Locate every Plasmodium parasite.
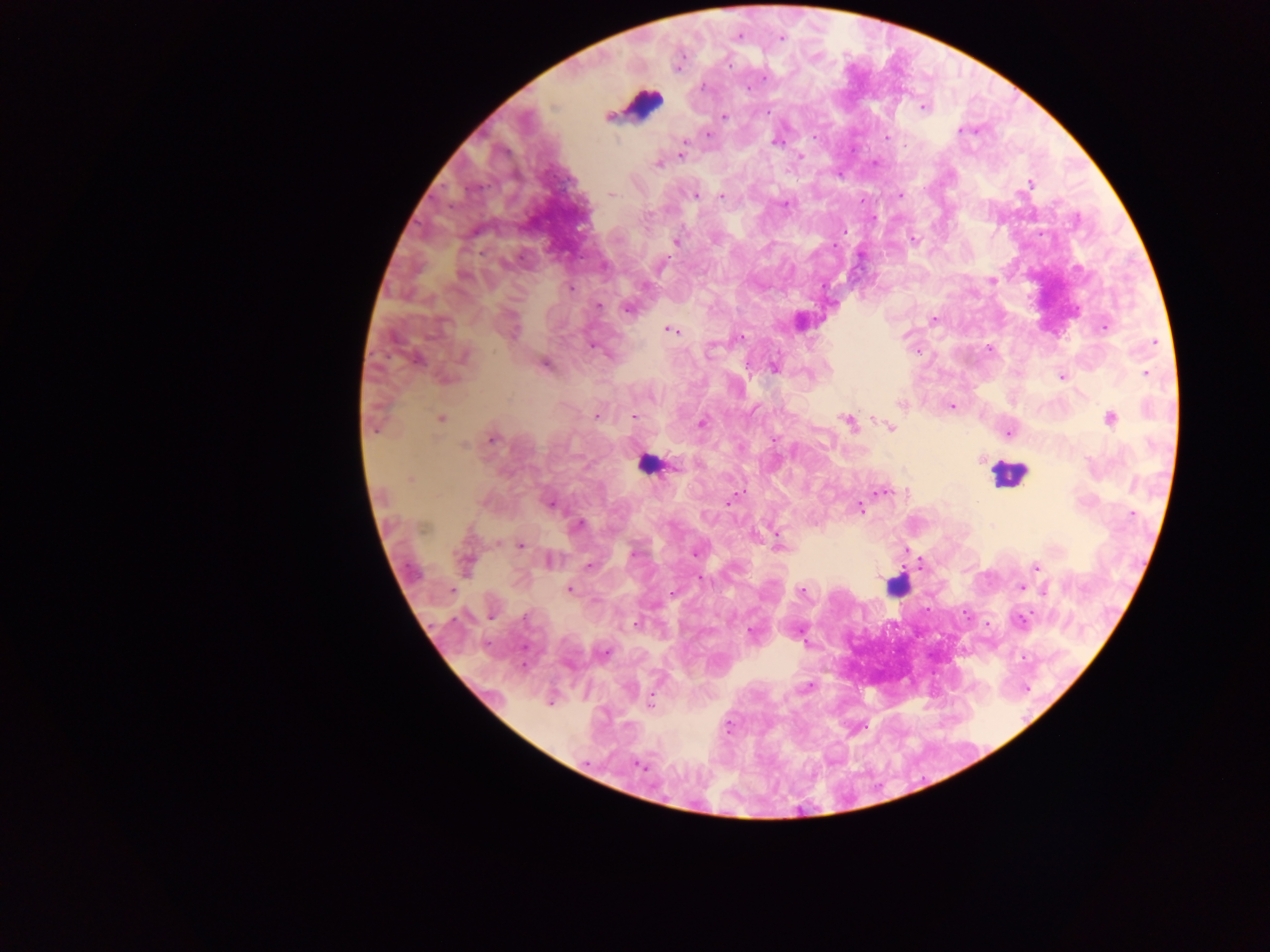

Approximate centers as x y in pixels.
Plasmodium parasites: 737 36; 780 39; 703 86; 747 88; 923 108; 766 113; 724 116; 961 129; 708 134; 887 136; 776 141; 686 143; 682 153; 800 156; 658 164; 1030 183; 611 195; 695 195; 900 195; 721 196; 785 204; 843 231; 914 239; 676 241; 661 265; 992 280; 571 288; 599 306; 627 309; 933 319; 1104 327; 670 330; 741 337; 591 346; 989 349; 709 352; 464 356; 416 359; 545 365; 775 369; 1146 373; 1061 376; 900 405; 952 405; 596 416; 634 417; 1110 418; 441 419; 848 421; 702 423; 375 427; 890 428; 1008 433; 492 439; 774 439; 465 444; 676 467; 410 480; 882 492; 730 500; 550 504; 860 508; 1132 514; 578 525; 423 527; 780 545; 520 546; 634 553; 695 553; 550 560; 465 563; 589 566; 1036 567; 700 579; 1020 587; 569 589; 451 590; 1045 590; 802 592; 672 594; 491 617; 1021 620; 636 624; 751 632; 804 641; 604 652; 807 688; 549 702; 651 704; 729 726; 638 766.

field of view = single
country = Ghana
leukocyte locations = approximate centers as x y in pixels: 642 104; 647 465; 1007 473; 897 585
capture = mobile-phone photograph through a microscope
image size = 1270×952 pixels
preparation = thick blood film